Classify this cell by malaria status.
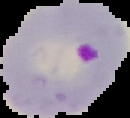

It is parasitized.

Summary:
  - Preparation: thin blood film
  - Image type: segmented cell region on a black background
  - Image size: 130×118 pixels